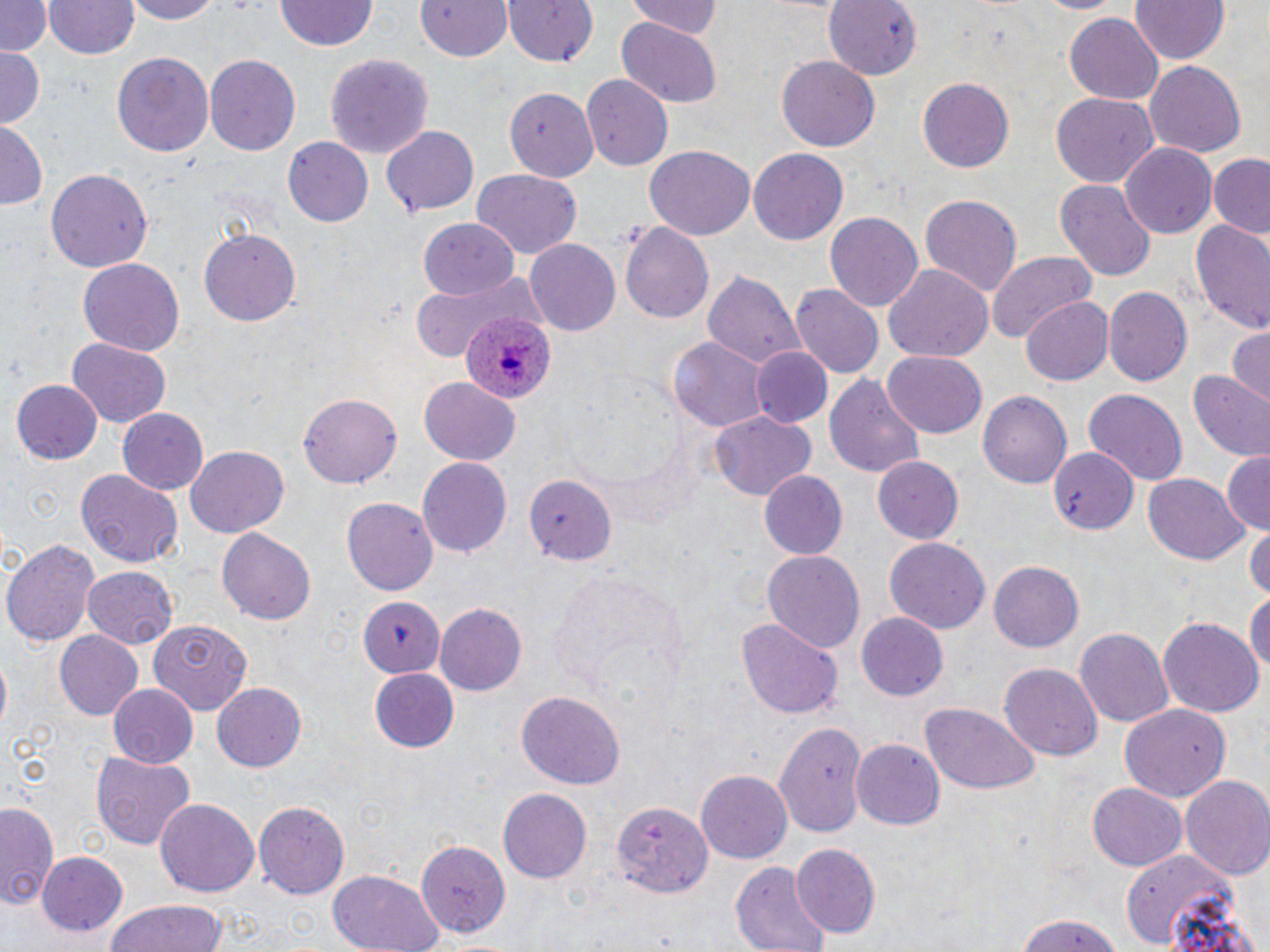 Approximate bounding boxes as (x1, y1, x2, y2) in pixels. Plasmodium ovale-infected red blood cell locations: (462, 311, 555, 405). Uninfected red blood cell locations: (0, 0, 53, 58), (43, 0, 141, 61), (122, 0, 223, 24), (277, 0, 377, 53), (417, 0, 515, 62), (503, 0, 600, 67), (626, 0, 722, 39), (821, 0, 923, 81), (1128, 0, 1230, 65), (1065, 14, 1162, 105), (613, 18, 725, 107), (0, 49, 44, 128), (112, 49, 214, 157), (326, 52, 433, 165), (205, 54, 303, 156), (778, 55, 879, 154), (1145, 61, 1247, 158), (583, 75, 674, 171), (917, 78, 1014, 171), (505, 86, 597, 180), (1050, 93, 1158, 189), (0, 122, 46, 208), (382, 127, 478, 216), (282, 137, 373, 227), (1119, 141, 1216, 236), (645, 145, 756, 241), (748, 147, 849, 246), (1208, 154, 1270, 238), (45, 168, 152, 273), (473, 171, 582, 257), (1056, 178, 1156, 281), (919, 192, 1024, 299), (826, 209, 925, 311), (420, 217, 520, 299), (1187, 217, 1270, 335), (621, 222, 713, 326), (197, 229, 299, 326), (525, 238, 621, 336), (986, 250, 1099, 341), (77, 258, 185, 356), (885, 265, 995, 363), (703, 270, 805, 373), (409, 273, 533, 362), (791, 286, 883, 376), (1104, 287, 1193, 387), (1023, 296, 1113, 386), (1228, 323, 1270, 402), (68, 337, 170, 427), (669, 337, 768, 431), (751, 348, 831, 429), (883, 353, 986, 437), (1186, 369, 1270, 462), (825, 375, 927, 479), (420, 378, 520, 465), (10, 379, 103, 465), (1082, 389, 1188, 485), (978, 390, 1071, 491), (298, 393, 402, 489), (117, 407, 210, 496), (707, 413, 816, 501), (187, 448, 287, 535), (1045, 448, 1139, 528), (1220, 451, 1270, 530), (870, 455, 964, 545), (418, 457, 513, 557), (75, 467, 184, 567), (758, 470, 847, 561), (1143, 473, 1249, 566), (525, 476, 617, 563), (342, 496, 439, 594), (1246, 525, 1270, 599), (217, 528, 316, 625), (1, 536, 100, 649), (884, 538, 988, 633), (763, 549, 865, 652), (989, 561, 1084, 651), (82, 566, 180, 645), (547, 569, 690, 696), (1246, 589, 1269, 686), (360, 597, 448, 677), (436, 603, 527, 696), (856, 612, 949, 701), (736, 616, 844, 720), (1158, 616, 1264, 717), (148, 620, 252, 713), (1075, 627, 1172, 730), (55, 631, 145, 721), (1001, 664, 1102, 761), (370, 668, 459, 751), (106, 682, 200, 767), (212, 682, 306, 773), (516, 690, 625, 789), (920, 702, 1040, 793), (1118, 702, 1231, 802), (774, 720, 865, 840), (851, 738, 943, 830), (91, 749, 197, 849), (696, 769, 793, 864), (1179, 775, 1270, 880), (1088, 781, 1187, 870), (498, 789, 592, 884), (156, 797, 260, 898), (255, 799, 351, 900), (613, 799, 712, 899), (0, 801, 62, 911), (414, 841, 509, 935), (790, 843, 879, 936), (1119, 849, 1245, 949), (38, 853, 129, 937), (732, 863, 832, 952), (327, 869, 444, 952), (103, 898, 229, 952), (1012, 913, 1129, 952). Slide-level diagnosis: Plasmodium ovale. Thin blood film. Image is 1270×952 pixels. Single field of view. Light microscopy. May-Grünwald-Giemsa-stained preparation. Captured at 1000x magnification.